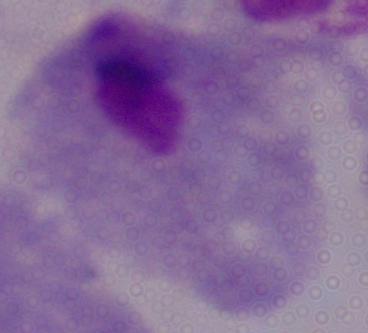 Captured at 1000x magnification. Photomicrograph. A trichomonad is shown.